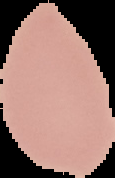
Summary:
  - Image size: 115×178 pixels
  - Preparation: thin blood film
  - Image type: cell region segmented out of the field of view; surrounding area masked to black
  - Malaria status: uninfected